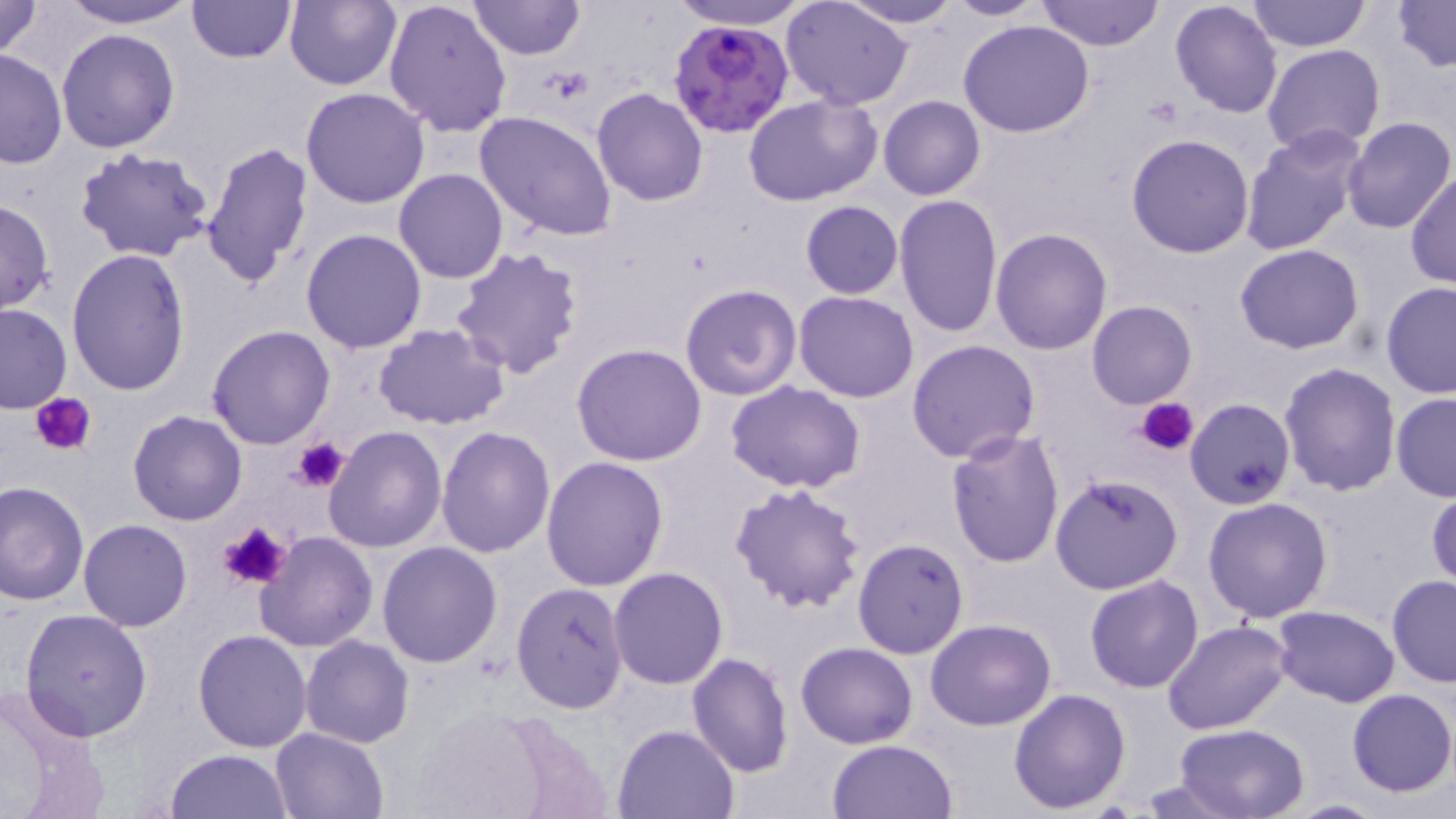

Summary:
  - Coordinate format: approximate bounding boxes as (x1, y1, x2, y2) in pixels
  - Platelet locations: (541, 68, 594, 103), (33, 393, 99, 456), (1139, 396, 1199, 454), (292, 438, 349, 493), (219, 523, 292, 593)
  - Uninfected red blood cell locations: (0, 0, 45, 60), (57, 0, 202, 27), (185, 0, 298, 64), (383, 0, 512, 138), (469, 0, 582, 60), (667, 0, 813, 30), (838, 0, 966, 28), (946, 0, 1045, 20), (1037, 0, 1165, 51), (1391, 0, 1455, 71), (283, 1, 401, 90), (781, 1, 913, 109), (1170, 1, 1284, 118), (1247, 1, 1370, 50), (959, 19, 1094, 137), (56, 29, 181, 153), (1262, 44, 1385, 155), (0, 49, 67, 169), (300, 87, 430, 209), (592, 88, 708, 206), (743, 94, 882, 205), (878, 95, 986, 201), (475, 111, 617, 241), (1340, 118, 1455, 235), (1240, 125, 1367, 257), (1126, 133, 1254, 258), (200, 140, 315, 292), (74, 146, 218, 265), (394, 169, 508, 284), (1406, 169, 1455, 290), (892, 194, 1003, 339), (0, 198, 54, 315), (800, 200, 904, 299), (300, 228, 428, 354), (990, 228, 1111, 355), (1234, 244, 1363, 353), (451, 246, 584, 379), (66, 248, 191, 395), (1381, 282, 1456, 399), (680, 283, 801, 402), (794, 290, 920, 402), (1087, 300, 1196, 408), (0, 303, 72, 413), (374, 323, 511, 430), (207, 325, 336, 447), (907, 340, 1041, 464), (572, 343, 707, 466), (1279, 363, 1402, 499), (725, 381, 865, 494), (1391, 393, 1456, 502), (128, 411, 247, 527), (323, 424, 448, 553), (436, 425, 556, 558), (945, 428, 1065, 569), (542, 456, 670, 591), (1049, 472, 1183, 593), (1, 481, 89, 607), (728, 482, 866, 613), (1427, 489, 1456, 592), (1202, 497, 1333, 623), (78, 519, 193, 632), (255, 531, 377, 652), (852, 537, 969, 659), (377, 541, 504, 667), (608, 567, 728, 689), (1084, 574, 1205, 693), (1386, 574, 1456, 688), (512, 583, 630, 716), (1271, 604, 1400, 707), (19, 608, 153, 742), (925, 619, 1057, 731), (1162, 619, 1293, 734), (192, 629, 311, 753), (301, 635, 414, 748), (796, 641, 919, 749), (686, 653, 794, 776), (0, 682, 107, 819), (1008, 688, 1131, 813), (1347, 688, 1455, 798), (414, 709, 555, 819), (1171, 722, 1312, 819), (612, 723, 739, 818), (270, 728, 389, 818), (828, 740, 957, 819), (167, 748, 293, 818)
  - Plasmodium falciparum-infected red blood cell locations: (666, 14, 796, 139)
  - Slide-level diagnosis: Plasmodium falciparum
  - Magnification: 1000x
  - Stain: May-Grünwald-Giemsa
  - Image size: 1456×819 pixels
  - Modality: light microscopy
  - Field of view: one of a larger specimen
  - Preparation: thin blood smear